Point out each Plasmodium parasite.
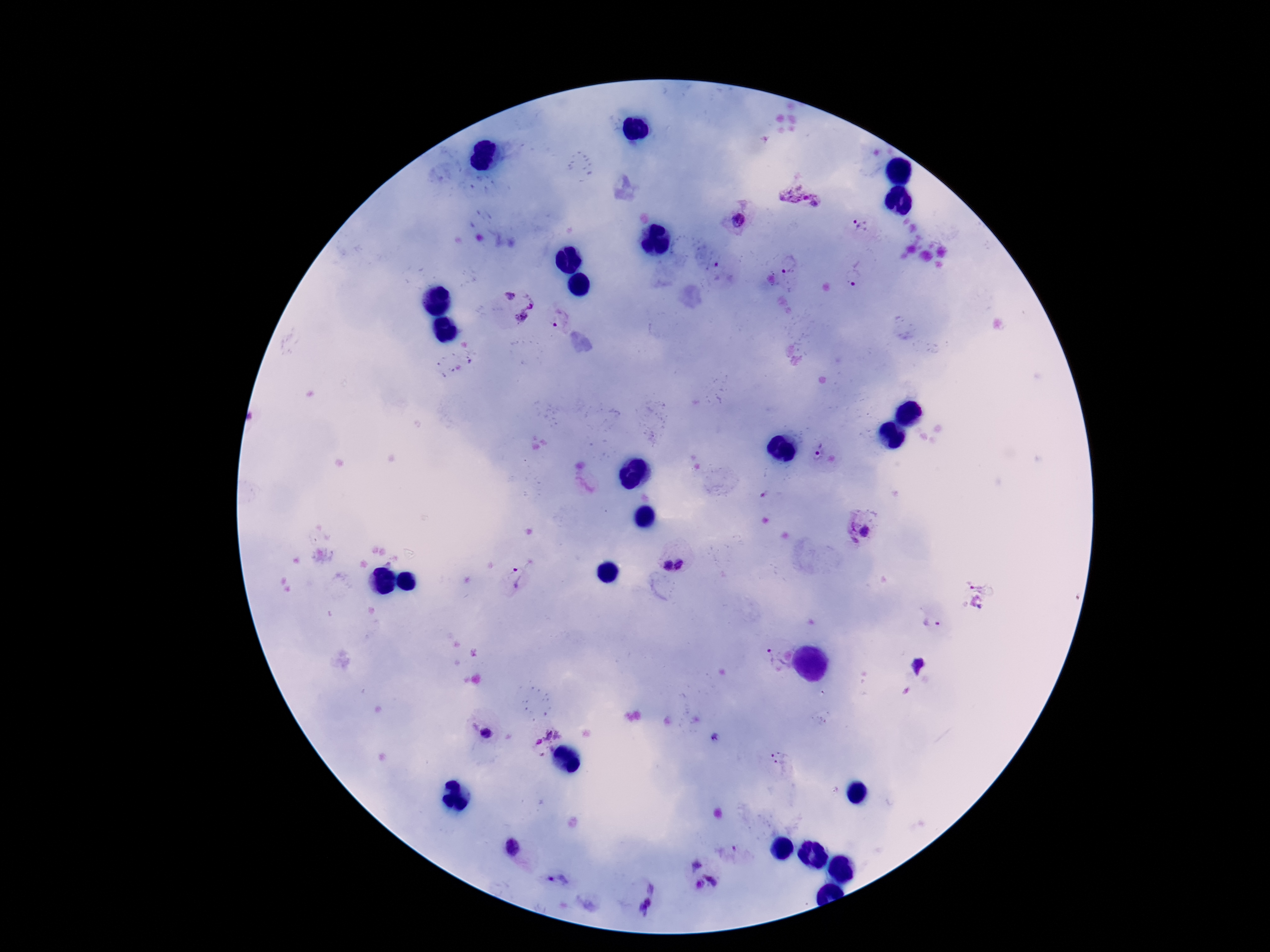
Approximate centers as {x, y} in pixels.
Plasmodium parasites: {799, 197}, {739, 221}, {861, 225}, {789, 264}, {857, 274}, {510, 296}, {529, 301}, {520, 318}, {556, 326}, {817, 452}, {864, 531}, {681, 565}, {666, 566}, {519, 578}, {932, 623}, {776, 658}, {485, 735}, {780, 758}, {511, 848}, {694, 866}, {713, 878}, {559, 881}, {698, 884}, {651, 887}, {646, 906}.

Summary:
  - Stain: Giemsa
  - Capture: smartphone camera through the microscope eyepiece
  - Patient malaria status: positive
  - Image size: 1270×952 pixels
  - Magnification: 100x
  - Preparation: thick peripheral-blood smear
  - Field of view: single